Identify the blood parasite species.
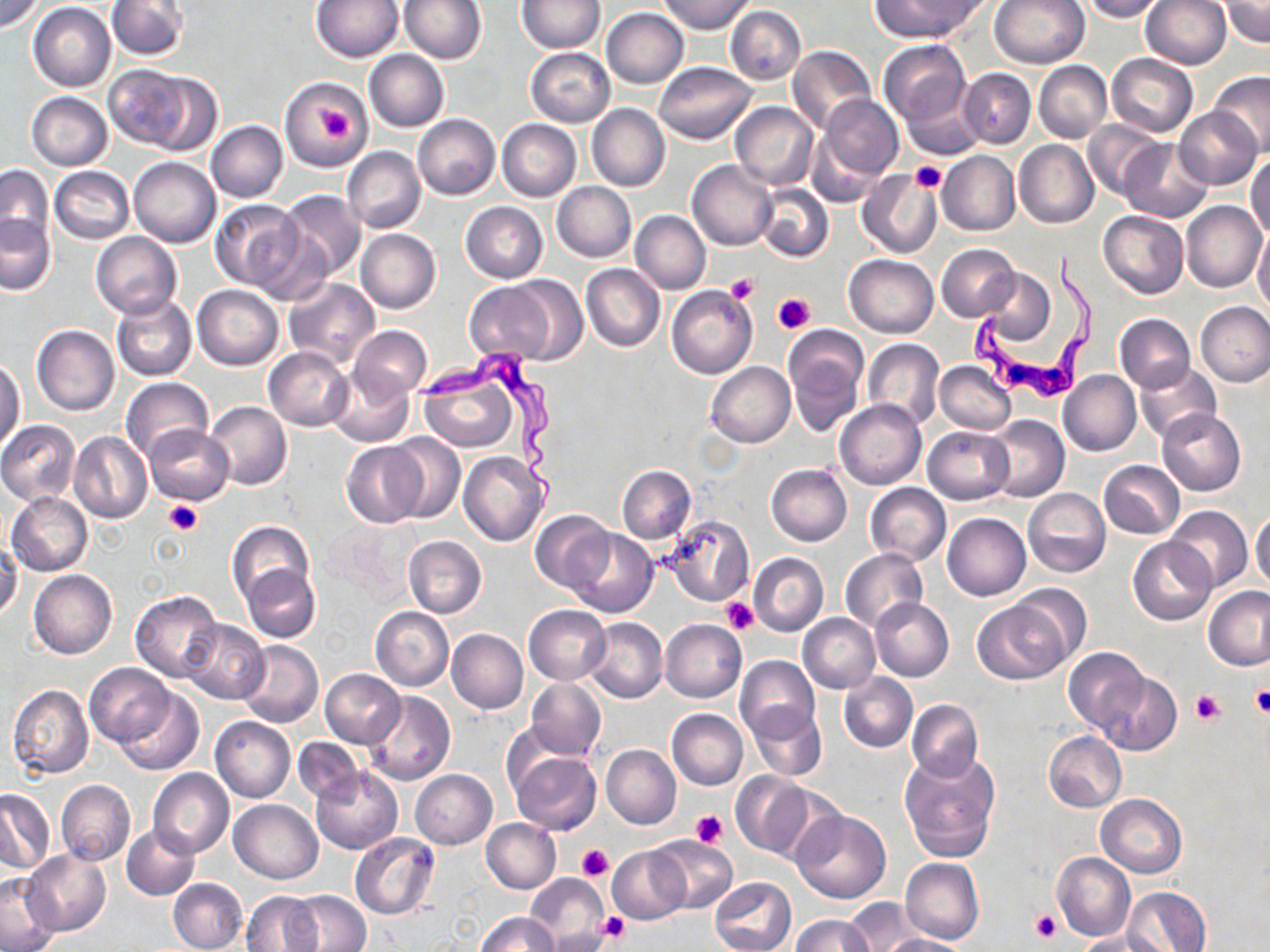
Trypanosoma brucei.

Approximate bounding boxes as (x1,y1)-(x2,y2) corner pairs in pixels. Uninfected red blood cell locations: (0,0)-(43,33), (106,0)-(188,60), (312,0)-(403,62), (401,0)-(485,62), (872,0)-(980,41), (990,0)-(1090,68), (1078,0)-(1166,21), (1141,0)-(1231,70), (517,1)-(604,53), (660,1)-(756,34), (1221,1)-(1269,47), (29,3)-(116,91), (726,5)-(805,85), (601,7)-(689,88), (879,40)-(970,125), (787,46)-(875,133), (526,48)-(615,126), (364,50)-(449,132), (1106,54)-(1197,137), (1035,61)-(1112,143), (653,62)-(755,143), (103,64)-(207,152), (959,68)-(1035,148), (1209,70)-(1270,159), (281,78)-(372,172), (901,87)-(985,161), (26,92)-(113,170), (40,95)-(122,245), (815,95)-(903,186), (730,102)-(818,189), (587,104)-(670,191), (1175,107)-(1261,189), (413,114)-(500,200), (497,119)-(581,202), (1082,120)-(1165,201), (206,121)-(288,202), (806,125)-(885,207), (1119,139)-(1213,222), (1014,140)-(1099,228), (342,146)-(425,233), (937,151)-(1020,235), (1246,156)-(1270,239), (129,157)-(221,248), (688,159)-(779,250), (1,165)-(54,245), (50,166)-(133,244), (858,169)-(944,258), (552,181)-(637,262), (756,182)-(833,263), (277,190)-(366,280), (212,200)-(305,291), (1181,200)-(1267,293), (461,202)-(548,283), (631,209)-(710,295), (1101,211)-(1188,298), (0,214)-(55,295), (251,226)-(334,305), (1253,227)-(1270,315), (355,229)-(440,313), (92,232)-(181,318), (937,244)-(1019,321), (845,254)-(938,338), (582,264)-(665,352), (979,267)-(1055,343), (503,276)-(588,364), (283,278)-(380,369), (463,280)-(558,364), (193,284)-(283,370), (667,285)-(757,379), (112,296)-(196,381), (1195,302)-(1270,387), (1115,314)-(1195,392), (31,325)-(119,416), (347,325)-(431,401), (785,329)-(865,434), (863,339)-(944,429), (263,346)-(355,431), (1,357)-(25,449), (934,361)-(1015,435), (1134,361)-(1222,443), (706,362)-(795,447), (419,367)-(520,453), (328,369)-(415,448), (1058,369)-(1141,457), (121,375)-(212,463), (834,399)-(926,489), (204,401)-(292,490), (1157,409)-(1246,495), (985,415)-(1070,502), (0,420)-(81,506), (143,425)-(235,504), (923,425)-(1015,504), (68,431)-(152,523), (384,434)-(465,524), (341,442)-(427,528), (458,451)-(549,546), (1099,460)-(1185,538), (767,464)-(852,546), (616,465)-(697,543), (865,483)-(950,565), (1023,487)-(1111,578), (6,492)-(93,576), (1165,505)-(1253,593), (1250,508)-(1270,591), (531,510)-(613,592), (942,513)-(1031,601), (660,514)-(755,606), (226,521)-(315,611), (316,522)-(411,611), (568,529)-(657,618), (403,535)-(486,618), (1127,536)-(1215,626), (0,541)-(22,621), (840,549)-(929,633), (749,553)-(828,636), (242,564)-(321,642), (28,569)-(118,660), (1010,583)-(1092,668), (1203,586)-(1270,672), (130,589)-(223,683), (971,597)-(1068,684), (870,598)-(954,681), (524,606)-(611,685), (371,607)-(454,690), (798,614)-(879,693), (180,618)-(269,704), (584,618)-(668,704), (660,619)-(747,703), (446,629)-(528,713), (238,640)-(323,727), (1062,646)-(1149,735), (736,655)-(819,739), (85,662)-(176,746), (321,669)-(405,748), (1096,669)-(1181,753), (838,671)-(917,753), (527,679)-(606,758), (7,684)-(94,779), (116,687)-(204,776), (364,690)-(454,786), (906,699)-(984,779), (746,702)-(826,782), (667,709)-(748,790), (210,716)-(295,802), (1042,731)-(1126,812), (292,738)-(363,803), (601,745)-(681,828), (509,748)-(602,835), (899,752)-(1000,862), (309,765)-(403,854), (149,768)-(234,858), (410,769)-(497,848), (730,772)-(812,857), (55,779)-(135,867), (0,791)-(54,874), (1094,794)-(1186,878), (229,800)-(323,884), (793,810)-(889,903), (482,819)-(560,893), (122,824)-(201,900), (349,832)-(440,920), (649,836)-(739,914), (608,845)-(690,924), (23,850)-(111,936), (1051,852)-(1135,940), (900,857)-(984,945), (0,872)-(59,951), (525,873)-(610,949), (709,876)-(797,952), (169,877)-(248,952), (1121,886)-(1212,952), (289,890)-(371,952), (241,891)-(324,952), (843,897)-(919,950), (478,912)-(559,952), (791,914)-(874,951), (547,926)-(612,952), (1075,931)-(1173,952), (881,934)-(972,952). Platelet locations: (319,102)-(355,140), (910,162)-(947,193), (726,273)-(761,305), (774,293)-(815,335), (165,501)-(203,536), (721,596)-(760,635), (1249,686)-(1270,717), (1191,691)-(1225,726), (691,809)-(729,847), (577,844)-(614,881), (1029,908)-(1061,944), (598,911)-(631,943). Trypanosoma brucei locations: (968,248)-(1096,402), (416,347)-(559,519). One field of a larger specimen. May-Grünwald-Giemsa stain. Image is 1270×952 pixels. 1000x magnification. Thin blood smear. Optical microscopy.